Report the malaria status of this cell.
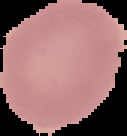

It is uninfected.

From a thin blood film. The area outside the segmented cell region is set to black. Image is 127×136 pixels.